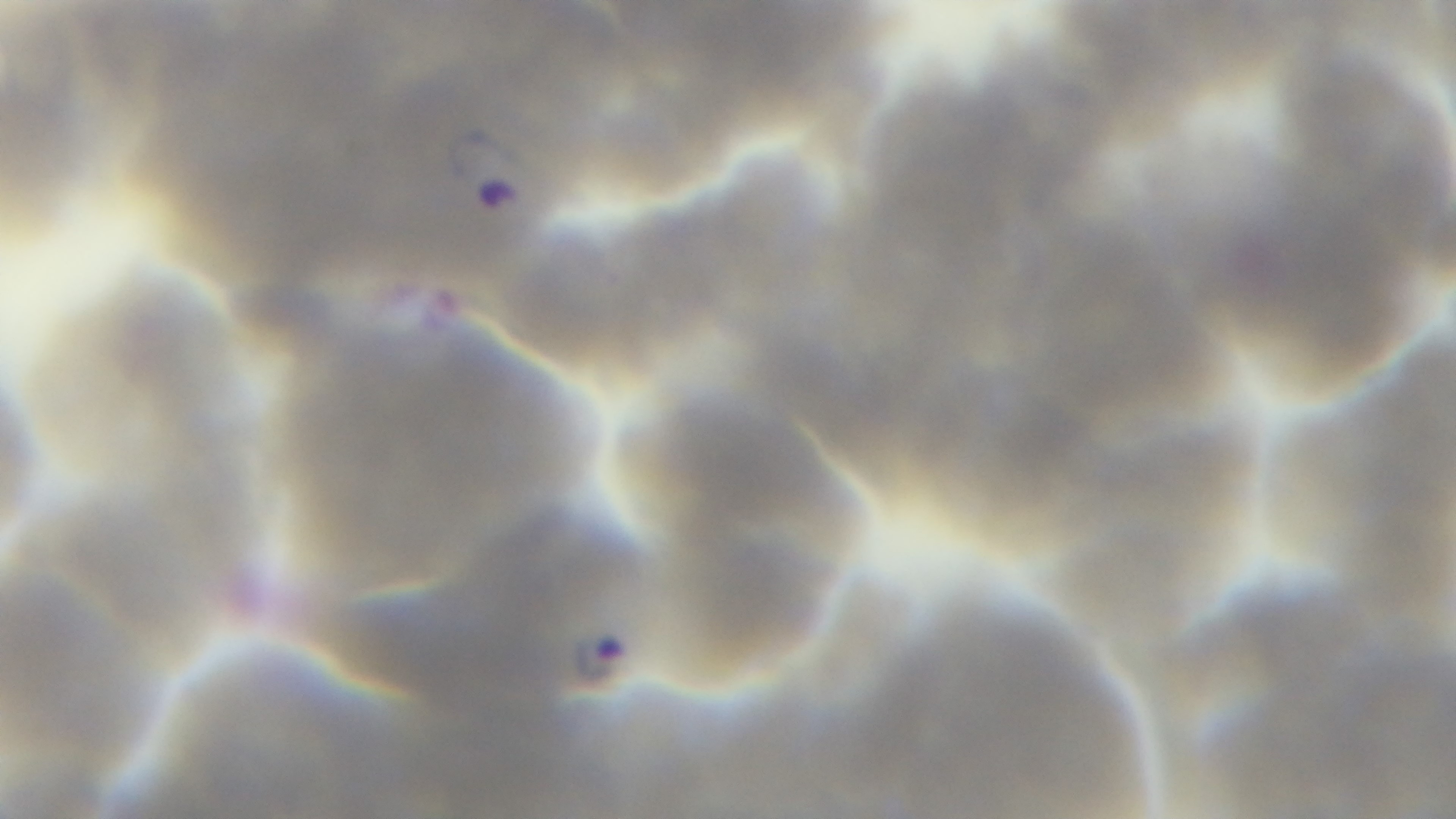
field of view = one from the slide
modality = light microscopy
objective = 100x oil immersion
preparation = thin
malaria status = infected
capture = mounted 4K digital camera
stain = Giemsa